Assess this cell for malaria.
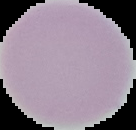
Uninfected.

From a thin blood smear. The area outside the segmented cell region is set to black. Image is 136×130 pixels.